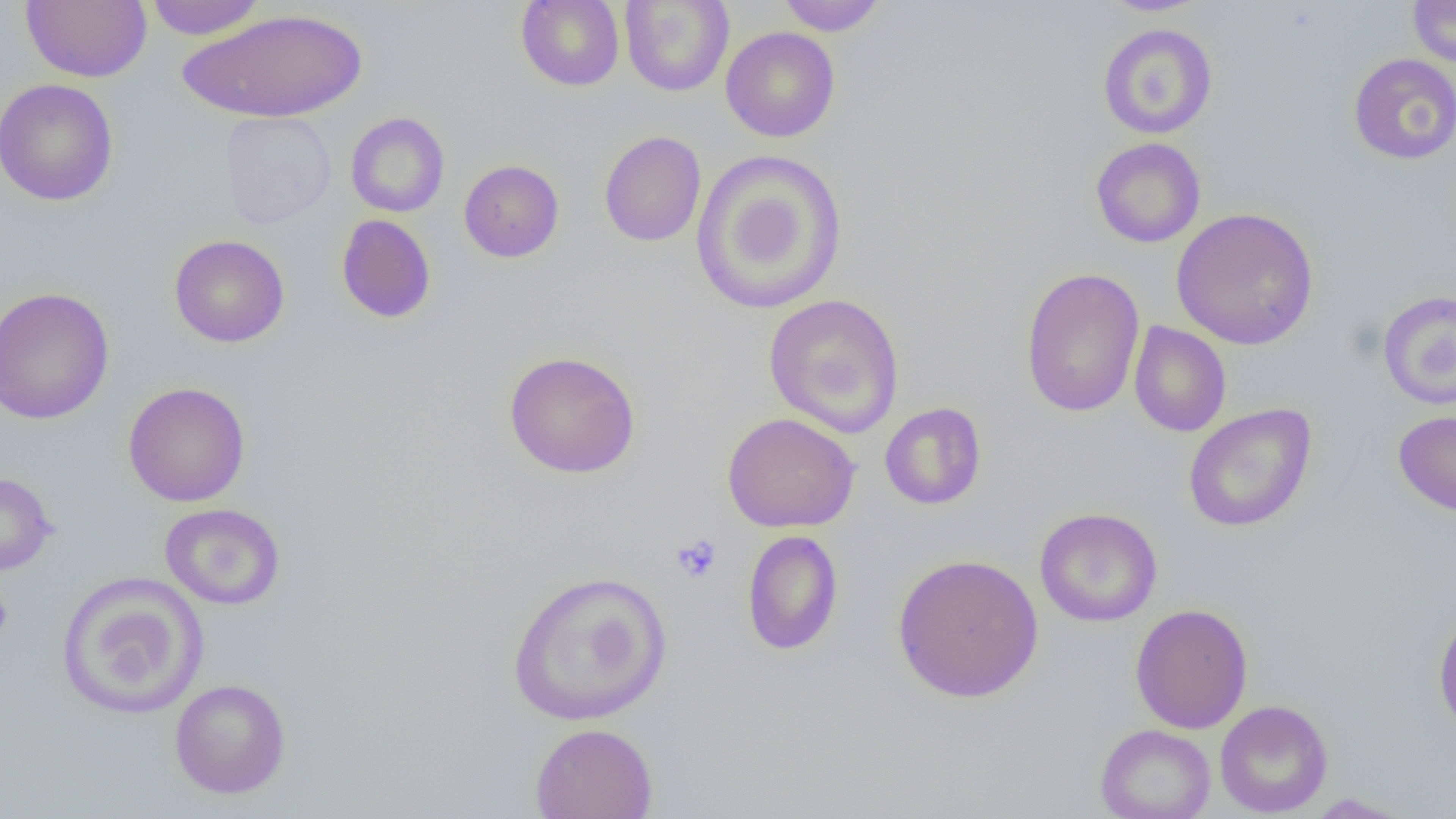

Summary:
  - Coordinate format: approximate bounding boxes as named x1/y1/x2/y2 corners in pixels
  - Uninfected red blood cell locations: (x1=20, y1=0, x2=152, y2=83), (x1=143, y1=0, x2=268, y2=40), (x1=515, y1=0, x2=625, y2=91), (x1=776, y1=0, x2=887, y2=36), (x1=1099, y1=0, x2=1213, y2=16), (x1=1407, y1=0, x2=1456, y2=67), (x1=619, y1=1, x2=734, y2=97), (x1=178, y1=8, x2=367, y2=123), (x1=1098, y1=23, x2=1217, y2=140), (x1=720, y1=26, x2=840, y2=142), (x1=1348, y1=53, x2=1456, y2=164), (x1=0, y1=78, x2=119, y2=206), (x1=219, y1=111, x2=336, y2=229), (x1=345, y1=112, x2=449, y2=217), (x1=598, y1=131, x2=706, y2=247), (x1=1090, y1=137, x2=1206, y2=248), (x1=691, y1=149, x2=849, y2=315), (x1=458, y1=159, x2=564, y2=263), (x1=1171, y1=207, x2=1319, y2=350), (x1=336, y1=214, x2=436, y2=323), (x1=169, y1=234, x2=290, y2=348), (x1=1020, y1=267, x2=1145, y2=417), (x1=0, y1=287, x2=115, y2=425), (x1=1377, y1=290, x2=1456, y2=410), (x1=763, y1=293, x2=905, y2=438), (x1=1129, y1=321, x2=1231, y2=437), (x1=503, y1=350, x2=641, y2=478), (x1=123, y1=382, x2=251, y2=507), (x1=880, y1=402, x2=987, y2=510), (x1=1182, y1=402, x2=1317, y2=532), (x1=1393, y1=410, x2=1456, y2=515), (x1=721, y1=412, x2=859, y2=533), (x1=0, y1=472, x2=56, y2=575), (x1=160, y1=503, x2=285, y2=610), (x1=1034, y1=507, x2=1162, y2=627), (x1=741, y1=530, x2=843, y2=655), (x1=891, y1=553, x2=1044, y2=703), (x1=506, y1=569, x2=672, y2=726), (x1=56, y1=573, x2=208, y2=719), (x1=1130, y1=603, x2=1253, y2=733), (x1=1433, y1=609, x2=1456, y2=736), (x1=169, y1=678, x2=291, y2=798), (x1=1214, y1=699, x2=1332, y2=817), (x1=529, y1=722, x2=658, y2=819), (x1=1095, y1=724, x2=1216, y2=819), (x1=1302, y1=793, x2=1414, y2=818)
  - Platelet locations: (x1=671, y1=534, x2=722, y2=583), (x1=0, y1=581, x2=13, y2=649)
  - Slide-level diagnosis: negative for blood parasites
  - Field of view: one of a larger specimen
  - Magnification: 1000x
  - Image size: 1456×819 pixels
  - Modality: light microscopy
  - Preparation: thin blood film